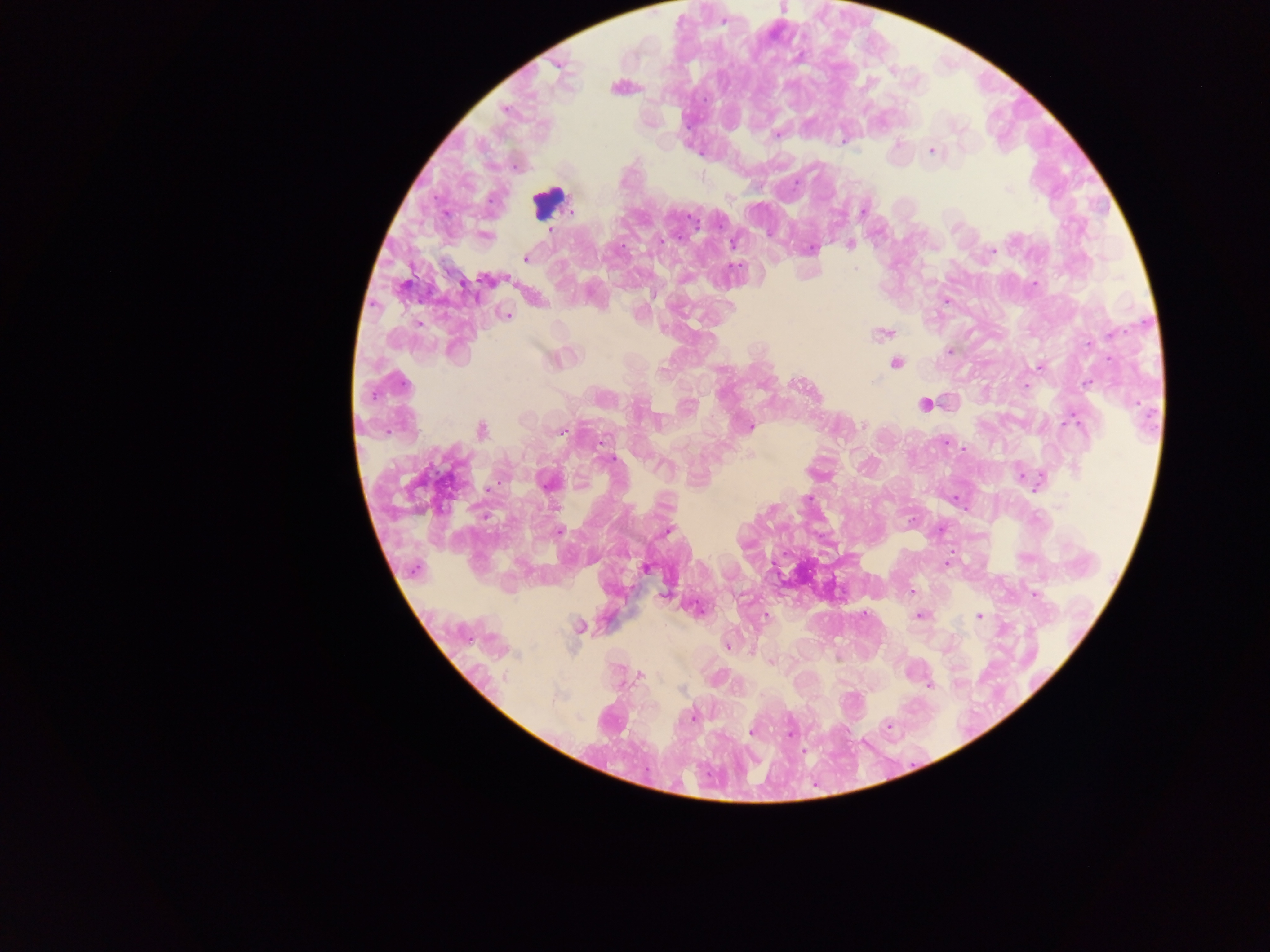

Approximate centers as [x, y] in pixels.
Summary:
  - Malaria parasite locations: [723, 24], [776, 134], [844, 137], [930, 151], [1006, 190], [862, 208], [849, 243], [733, 244], [810, 247], [990, 250], [524, 258], [510, 280], [1035, 282], [945, 301], [508, 313], [417, 322], [694, 322], [880, 334], [948, 351], [895, 363], [1037, 366], [872, 382], [1024, 386], [923, 404], [862, 425], [1071, 425], [480, 430], [559, 431], [603, 438], [944, 442], [609, 458], [1020, 473], [548, 482], [1036, 487], [489, 488], [769, 509], [668, 530], [560, 531], [564, 536], [1026, 557], [947, 563], [644, 567], [912, 591], [1035, 593], [919, 615], [978, 615], [763, 616], [863, 617], [580, 626], [728, 644], [836, 659], [771, 662], [640, 676], [959, 681], [930, 687], [619, 688], [683, 690], [692, 718], [888, 728], [751, 733], [788, 734], [805, 749]
  - Field of view: single
  - Country: Ghana
  - Image size: 1270×952 pixels
  - Preparation: thick blood smear
  - Capture: mobile-phone photograph through a microscope